State which cell type is depicted.
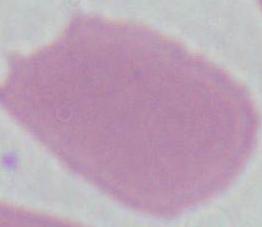

This is an erythrocyte.

Summary:
  - Modality: micrograph
  - Magnification: 1000x